Classify the preparation.
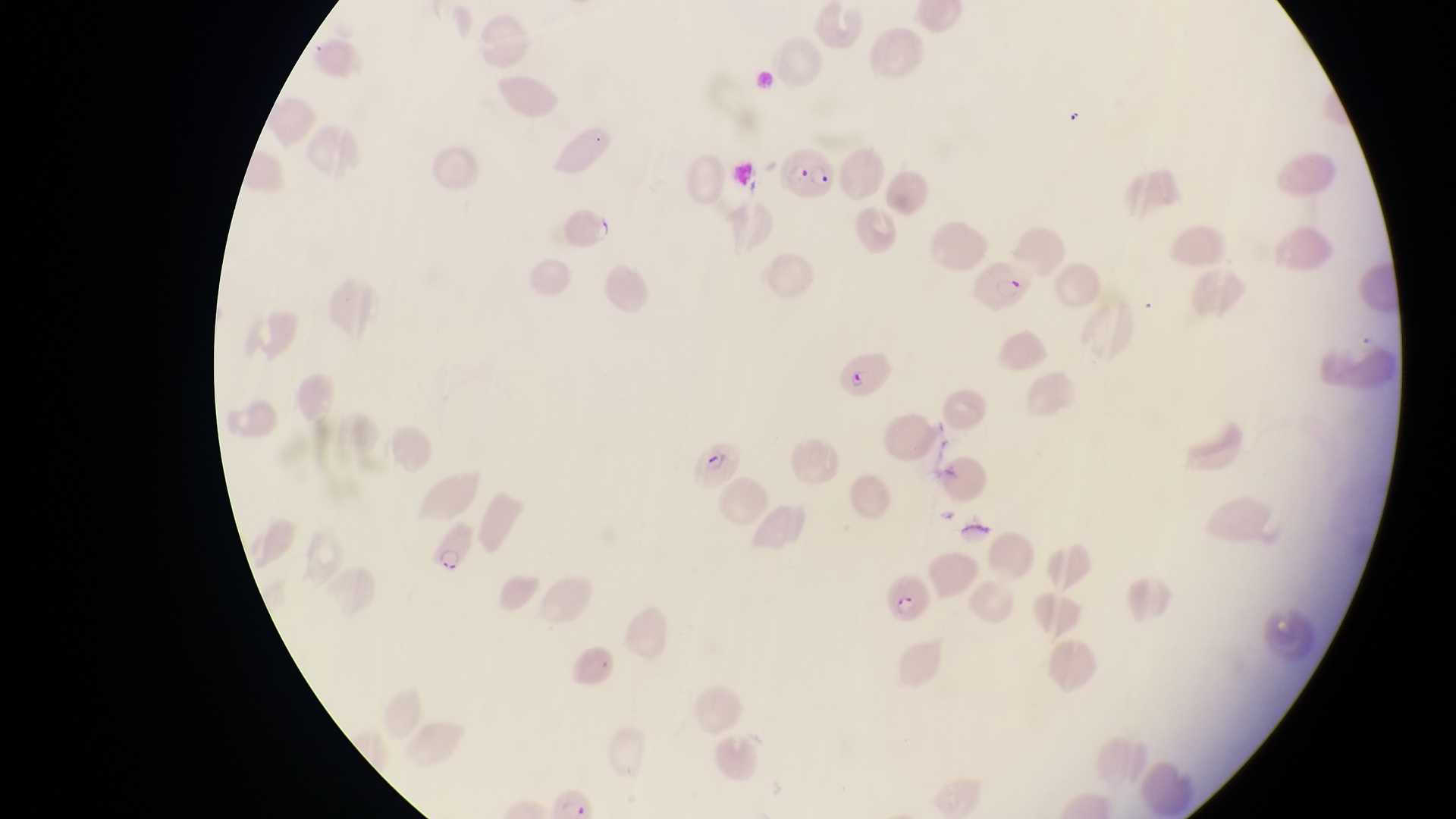
Thin blood smear.

Approximate bounding boxes as left top right bottom in pixels.
Summary:
  - Parasitised red blood cell locations: 782 149 837 199; 967 256 1036 319; 830 341 897 401; 689 436 744 488; 420 525 479 577; 880 570 936 629; 547 786 593 815
  - Magnification: 1000x
  - Field of view: single
  - Capture: smartphone photograph through the eyepiece of an Olympus CX-23 microscope
  - Country: Uganda
  - Image size: 1456×819 pixels